Report the malaria status of this cell.
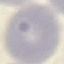
Uninfected.

{
  "capture": "smartphone through the microscope eyepiece",
  "preparation": "thin blood smear",
  "stain": "Giemsa",
  "image_type": "cell patch, automatically extracted from a larger field of view and resized to 64 × 64 pixels"
}